State the blood parasite species.
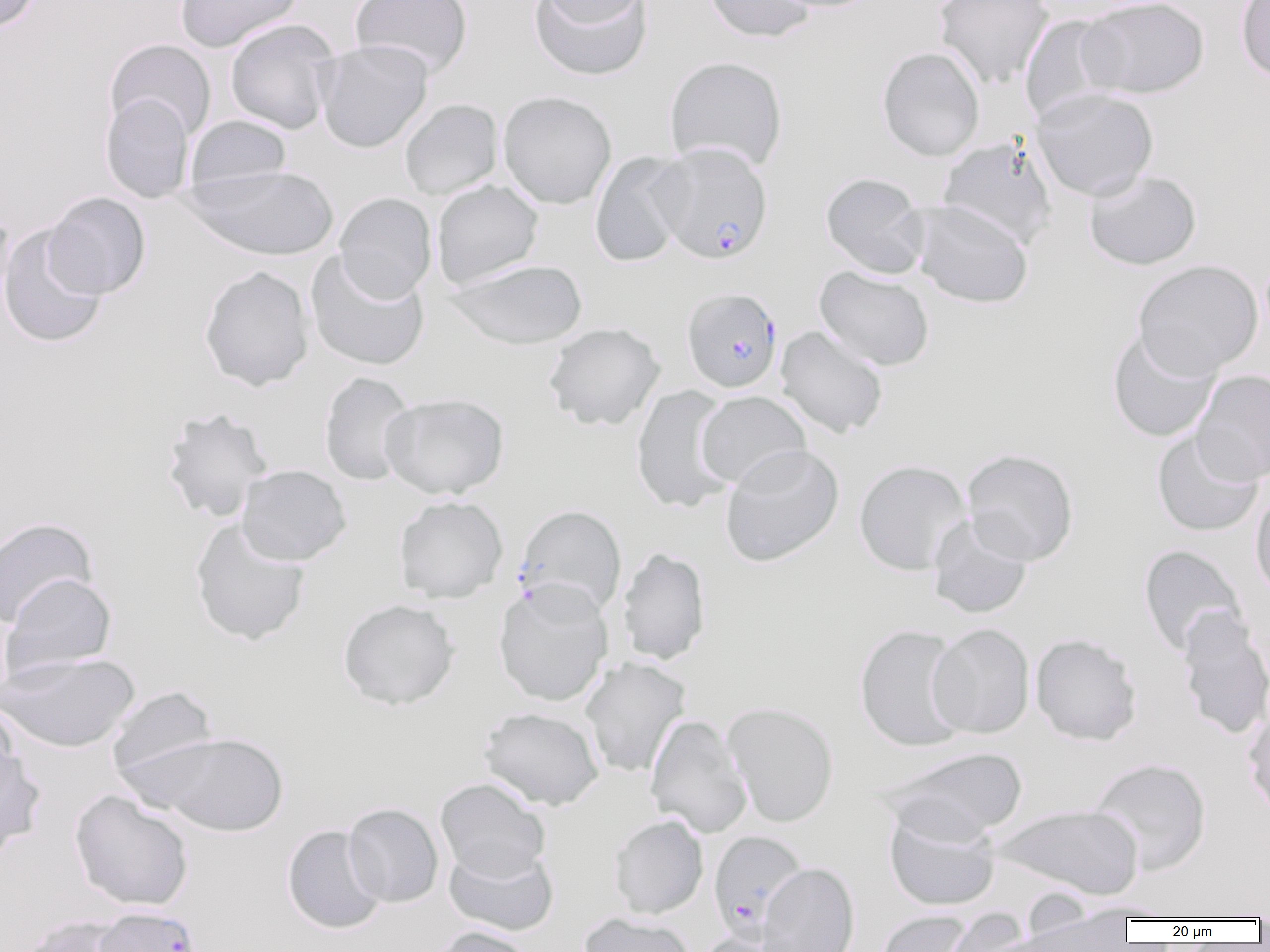
Plasmodium falciparum.

Summary:
  - Coordinate format: approximate bounding boxes as named x1/y1/x2/y2 corners in pixels
  - Uninfected red blood cell locations: (x1=0, y1=0, x2=42, y2=31), (x1=174, y1=0, x2=303, y2=52), (x1=349, y1=0, x2=473, y2=79), (x1=537, y1=0, x2=651, y2=26), (x1=704, y1=0, x2=816, y2=43), (x1=768, y1=0, x2=884, y2=13), (x1=934, y1=0, x2=1053, y2=90), (x1=1078, y1=0, x2=1210, y2=99), (x1=1236, y1=0, x2=1270, y2=83), (x1=528, y1=1, x2=654, y2=81), (x1=1019, y1=14, x2=1120, y2=125), (x1=224, y1=19, x2=341, y2=135), (x1=105, y1=39, x2=216, y2=141), (x1=315, y1=39, x2=434, y2=153), (x1=877, y1=46, x2=985, y2=161), (x1=664, y1=56, x2=787, y2=172), (x1=1031, y1=87, x2=1159, y2=201), (x1=497, y1=91, x2=617, y2=209), (x1=100, y1=93, x2=195, y2=204), (x1=399, y1=98, x2=503, y2=199), (x1=185, y1=115, x2=291, y2=195), (x1=938, y1=136, x2=1058, y2=249), (x1=589, y1=150, x2=691, y2=268), (x1=182, y1=163, x2=339, y2=261), (x1=1083, y1=168, x2=1201, y2=271), (x1=820, y1=172, x2=930, y2=279), (x1=431, y1=180, x2=544, y2=289), (x1=44, y1=192, x2=150, y2=298), (x1=334, y1=192, x2=437, y2=302), (x1=911, y1=199, x2=1034, y2=308), (x1=0, y1=206, x2=15, y2=322), (x1=0, y1=224, x2=109, y2=348), (x1=305, y1=251, x2=430, y2=371), (x1=445, y1=259, x2=589, y2=350), (x1=1133, y1=260, x2=1263, y2=379), (x1=199, y1=265, x2=314, y2=391), (x1=814, y1=265, x2=935, y2=371), (x1=543, y1=322, x2=665, y2=431), (x1=775, y1=325, x2=888, y2=439), (x1=1106, y1=327, x2=1222, y2=443), (x1=1191, y1=370, x2=1270, y2=485), (x1=319, y1=371, x2=417, y2=486), (x1=631, y1=384, x2=737, y2=514), (x1=695, y1=390, x2=811, y2=488), (x1=380, y1=393, x2=509, y2=500), (x1=160, y1=407, x2=275, y2=523), (x1=1152, y1=429, x2=1264, y2=537), (x1=720, y1=444, x2=844, y2=567), (x1=962, y1=448, x2=1079, y2=565), (x1=853, y1=459, x2=972, y2=575), (x1=236, y1=464, x2=351, y2=565), (x1=1250, y1=487, x2=1270, y2=602), (x1=393, y1=496, x2=508, y2=603), (x1=927, y1=514, x2=1034, y2=618), (x1=0, y1=516, x2=97, y2=628), (x1=190, y1=517, x2=311, y2=646), (x1=1138, y1=545, x2=1247, y2=657), (x1=617, y1=547, x2=711, y2=665), (x1=1, y1=572, x2=117, y2=678), (x1=493, y1=581, x2=614, y2=707), (x1=337, y1=599, x2=460, y2=710), (x1=0, y1=603, x2=15, y2=707), (x1=1176, y1=607, x2=1270, y2=741), (x1=927, y1=623, x2=1035, y2=739), (x1=853, y1=624, x2=970, y2=752), (x1=1031, y1=633, x2=1142, y2=745), (x1=0, y1=652, x2=140, y2=753), (x1=580, y1=657, x2=690, y2=778), (x1=106, y1=685, x2=220, y2=788), (x1=0, y1=701, x2=21, y2=797), (x1=722, y1=701, x2=839, y2=827), (x1=479, y1=706, x2=605, y2=810), (x1=1243, y1=707, x2=1270, y2=820), (x1=645, y1=715, x2=753, y2=838), (x1=146, y1=731, x2=290, y2=836), (x1=0, y1=738, x2=46, y2=857), (x1=876, y1=746, x2=1029, y2=842), (x1=1088, y1=757, x2=1211, y2=875), (x1=435, y1=778, x2=551, y2=882), (x1=69, y1=790, x2=194, y2=912), (x1=343, y1=803, x2=443, y2=908), (x1=996, y1=803, x2=1144, y2=900), (x1=884, y1=807, x2=1000, y2=911), (x1=609, y1=815, x2=709, y2=919), (x1=282, y1=825, x2=387, y2=934), (x1=444, y1=843, x2=559, y2=936), (x1=756, y1=862, x2=860, y2=952), (x1=1063, y1=899, x2=1179, y2=919), (x1=941, y1=907, x2=1032, y2=952), (x1=875, y1=909, x2=976, y2=952), (x1=579, y1=912, x2=695, y2=952), (x1=1007, y1=912, x2=1134, y2=951), (x1=15, y1=916, x2=135, y2=952), (x1=429, y1=925, x2=535, y2=952), (x1=694, y1=933, x2=794, y2=952)
  - Plasmodium falciparum-infected red blood cell locations: (x1=652, y1=142, x2=774, y2=264), (x1=682, y1=287, x2=783, y2=393), (x1=514, y1=504, x2=627, y2=617), (x1=708, y1=831, x2=808, y2=942), (x1=93, y1=905, x2=202, y2=952)
  - Modality: light microscopy
  - Image size: 1270×952 pixels
  - Field of view: one of a larger specimen
  - Magnification: 1000x
  - Preparation: thin blood smear